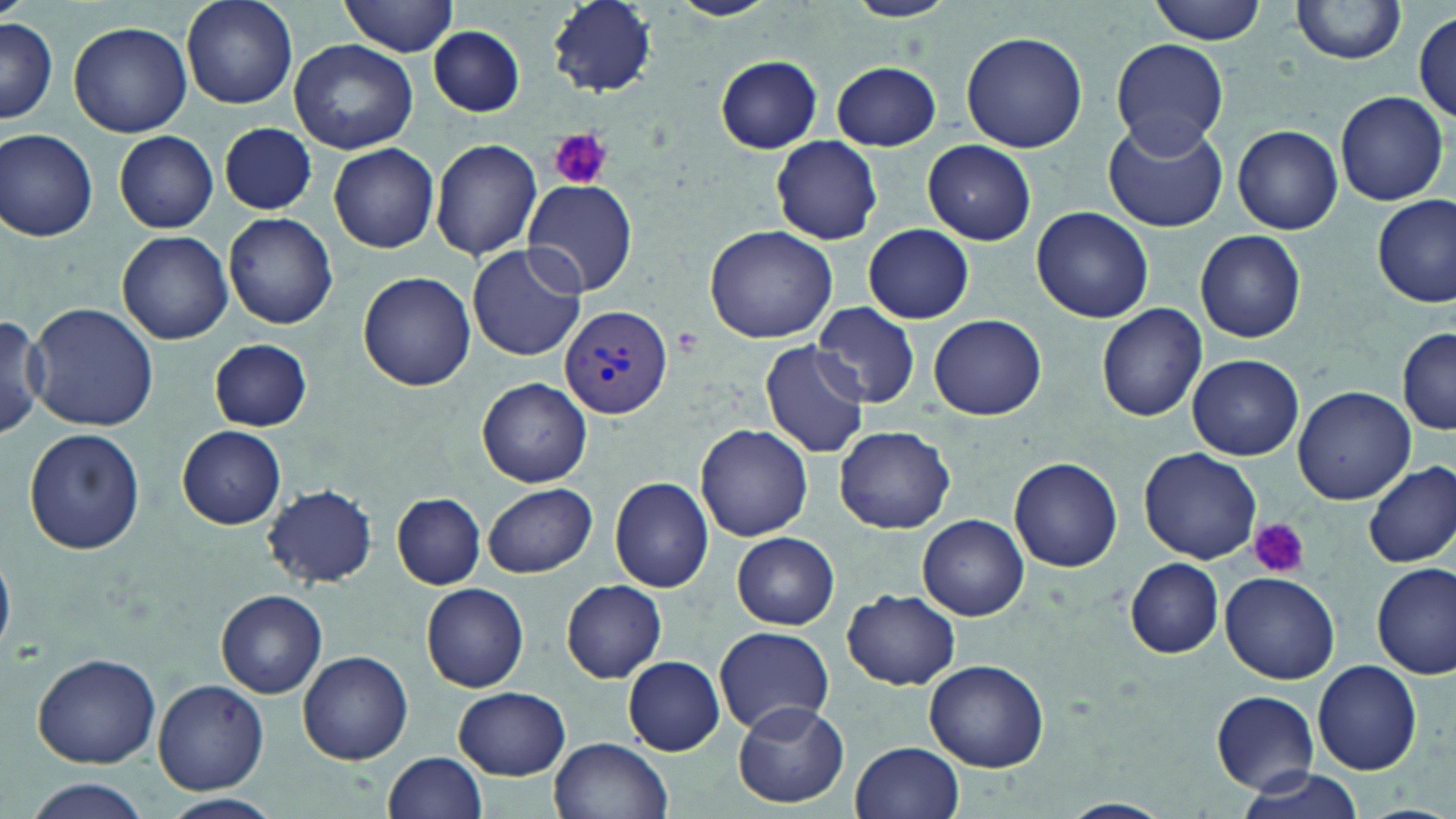
Approximate bounding boxes as (x1,y1)-(x2,y2) corner pairs in pixels. Plasmodium vivax-infected red blood cell locations: (560,304)-(672,422). Platelet locations: (551,129)-(613,190), (1249,518)-(1309,579). Uninfected red blood cell locations: (180,0)-(301,112), (340,0)-(460,58), (548,0)-(659,96), (665,0)-(783,21), (841,0)-(960,22), (1148,0)-(1270,44), (1290,1)-(1407,67), (1413,10)-(1456,123), (1,17)-(58,123), (68,21)-(191,136), (428,23)-(525,117), (961,31)-(1088,153), (289,38)-(418,153), (1110,39)-(1230,154), (715,55)-(823,154), (832,61)-(941,150), (1334,92)-(1448,206), (1102,116)-(1229,234), (216,122)-(321,217), (1232,125)-(1342,235), (1,128)-(99,242), (115,130)-(218,233), (770,136)-(882,244), (430,138)-(542,259), (924,140)-(1035,244), (329,143)-(440,253), (522,178)-(637,297), (1373,194)-(1455,308), (1031,207)-(1153,323), (224,213)-(337,328), (863,223)-(973,322), (704,224)-(840,345), (117,230)-(232,344), (1195,230)-(1307,343), (466,244)-(586,361), (357,271)-(477,391), (27,302)-(159,432), (812,302)-(919,409), (1097,303)-(1208,422), (0,312)-(45,443), (929,314)-(1046,421), (1398,328)-(1455,435), (209,338)-(314,431), (760,341)-(870,458), (1188,353)-(1304,459), (478,378)-(589,487), (1292,387)-(1416,504), (696,424)-(813,540), (834,426)-(955,533), (177,427)-(286,529), (22,428)-(145,555), (1141,448)-(1261,565), (1010,455)-(1123,572), (1364,462)-(1456,569), (609,475)-(713,593), (484,483)-(597,577), (264,484)-(377,588), (394,493)-(485,589), (919,515)-(1027,618), (732,531)-(839,631), (1125,558)-(1224,658), (1372,564)-(1454,678), (1219,572)-(1339,684), (561,579)-(667,683), (422,582)-(531,692), (217,589)-(327,697), (843,589)-(960,689), (713,626)-(835,733), (298,650)-(414,765), (32,652)-(162,767), (623,656)-(725,755), (924,659)-(1049,771), (1314,660)-(1423,774), (153,680)-(267,794), (453,687)-(570,780), (1212,691)-(1318,790), (731,702)-(850,808), (551,735)-(674,819), (851,741)-(964,819), (383,752)-(487,819), (1236,766)-(1362,819), (18,777)-(154,819), (159,794)-(283,818), (1055,800)-(1173,819). Slide-level diagnosis: Plasmodium vivax. One field of a larger specimen. Thin blood film. Captured at 1000x magnification. Image is 1456×819 pixels. Optical microscopy. May-Grünwald-Giemsa-stained preparation.